Locate every blood parasite and identify its species.
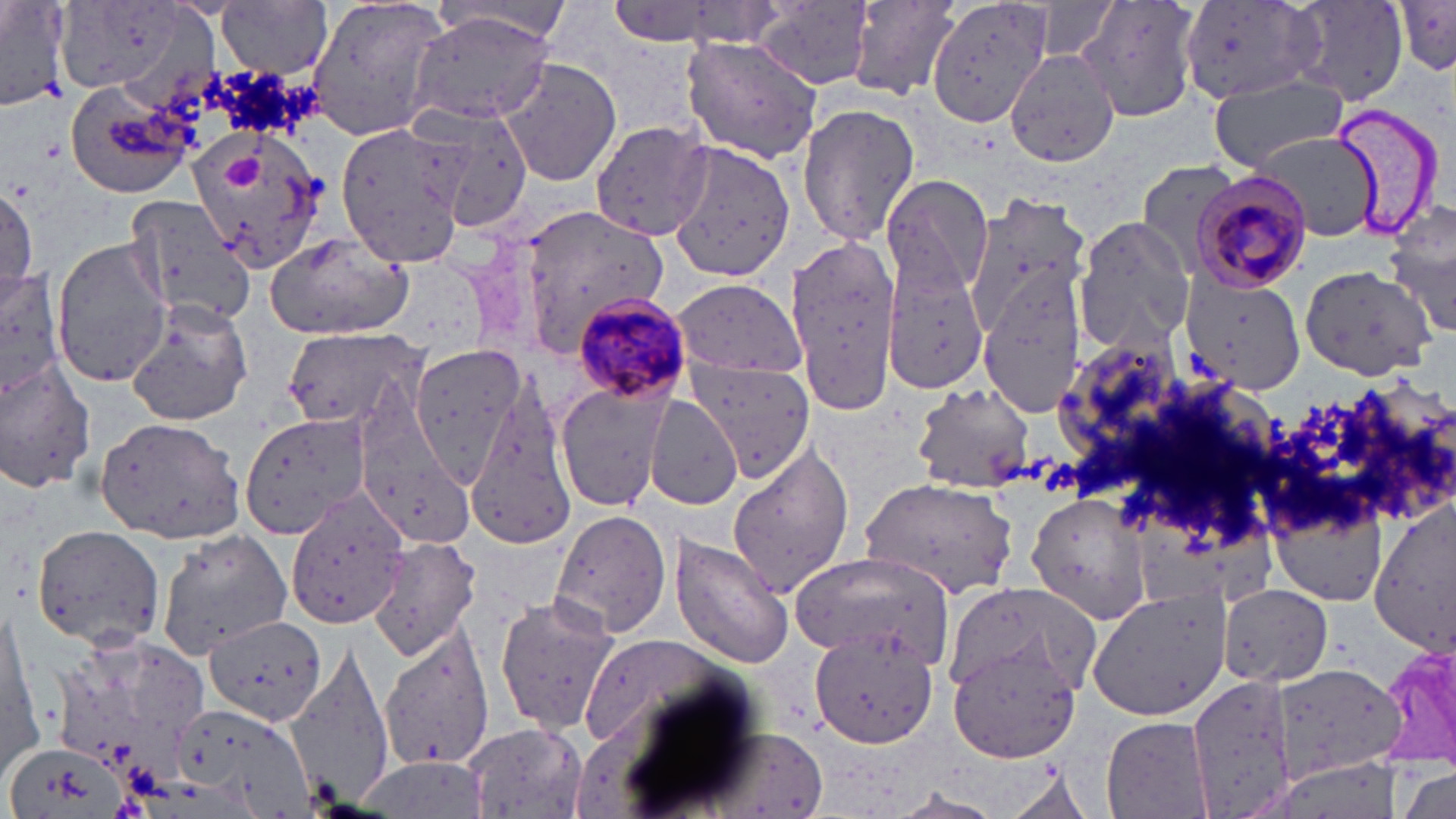
Approximate bounding boxes as [x1, y1, x2, y2] in pixels.
Plasmodium malariae-infected red blood cells: [1192, 171, 1313, 291], [569, 291, 692, 404].
No Plasmodium falciparum, Plasmodium ovale, Plasmodium vivax, Babesia divergens, or Trypanosoma brucei observed.

{
  "slide_level_diagnosis": "Plasmodium malariae",
  "magnification": "1000x",
  "uninfected_red_blood_cell_locations": "approximate bounding boxes as [x1, y1, x2, y2] in pixels: [0, 0, 70, 113], [304, 0, 453, 143], [845, 0, 962, 101], [926, 0, 1051, 128], [1074, 0, 1202, 123], [1282, 0, 1411, 107], [1392, 1, 1456, 74], [219, 2, 334, 78], [425, 2, 574, 44], [1179, 2, 1322, 104], [55, 3, 203, 101], [756, 3, 876, 89], [406, 12, 557, 127], [682, 35, 824, 162], [1006, 45, 1125, 172], [498, 60, 623, 186], [1209, 77, 1349, 170], [64, 82, 198, 199], [796, 100, 921, 249], [406, 104, 534, 232], [589, 118, 713, 244], [333, 121, 467, 269], [184, 126, 332, 273], [1253, 132, 1383, 243], [665, 139, 798, 284], [1133, 159, 1243, 278], [881, 175, 993, 302], [0, 186, 36, 300], [961, 192, 1089, 339], [124, 193, 257, 325], [1387, 207, 1456, 336], [516, 208, 665, 354], [1071, 217, 1197, 356], [786, 232, 901, 416], [264, 233, 412, 341], [51, 236, 172, 386], [882, 264, 991, 393], [1301, 264, 1436, 381], [0, 267, 65, 395], [979, 275, 1087, 413], [1181, 275, 1307, 393], [669, 278, 805, 377], [125, 301, 256, 425], [278, 323, 427, 436], [1052, 335, 1191, 468], [409, 342, 526, 477], [0, 357, 98, 496], [690, 360, 813, 480], [1264, 376, 1444, 539], [555, 383, 668, 512], [912, 384, 1034, 494], [647, 393, 746, 510], [463, 401, 579, 551], [241, 412, 368, 539], [94, 417, 245, 543], [361, 441, 474, 543], [727, 441, 857, 598], [862, 477, 1020, 599], [1024, 490, 1153, 626], [285, 494, 407, 630], [1266, 497, 1390, 604], [548, 506, 674, 640], [31, 525, 165, 654], [155, 528, 293, 655], [154, 529, 294, 659], [669, 533, 793, 670], [365, 538, 483, 663], [790, 553, 957, 665], [944, 582, 1100, 697], [1088, 584, 1230, 721], [1217, 586, 1335, 691], [493, 592, 621, 737], [1, 602, 43, 777], [203, 615, 327, 725], [380, 625, 497, 772], [47, 629, 208, 791], [809, 630, 941, 749], [575, 632, 736, 751], [947, 641, 1083, 766], [285, 644, 399, 811], [1274, 660, 1404, 782], [1172, 675, 1296, 818], [168, 698, 316, 816], [1102, 716, 1213, 817], [464, 723, 587, 816], [5, 740, 121, 819], [1397, 769, 1454, 819]",
  "platelet_locations": "approximate bounding boxes as [x1, y1, x2, y2] in pixels: [223, 156, 266, 191]",
  "stain": "May-Grünwald-Giemsa",
  "image_size": "1456×819 pixels",
  "preparation": "thin blood film",
  "field_of_view": "single",
  "modality": "light microscopy"
}